Give the extent of all Plasmodium falciparum-infected red blood cells.
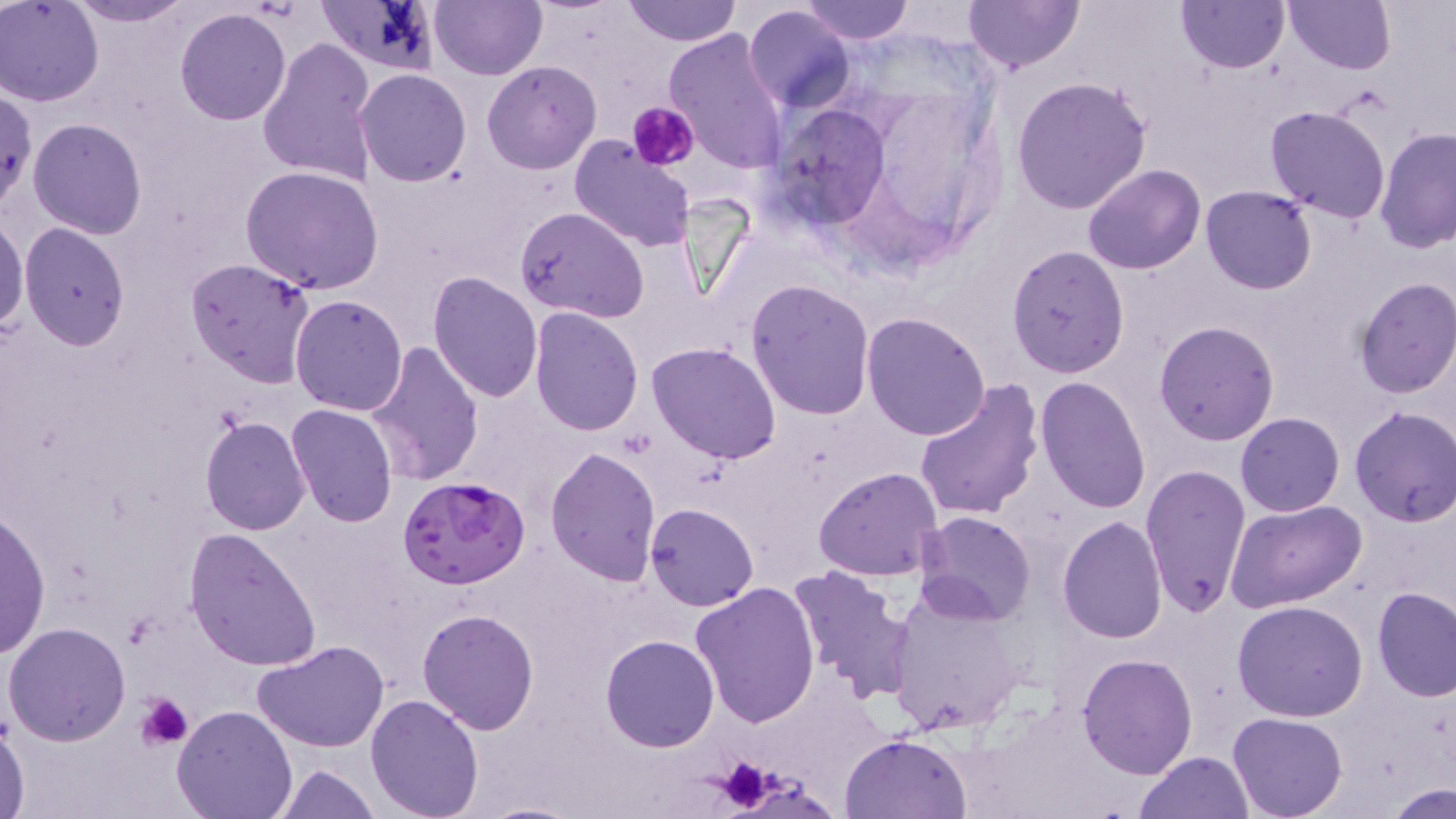

Approximate bounding boxes as named x1/y1/x2/y2 corners in pixels.
Plasmodium falciparum-infected red blood cells: (x1=397, y1=475, x2=530, y2=590).

slide-level diagnosis = Plasmodium falciparum
uninfected red blood cell locations = approximate bounding boxes as named x1/y1/x2/y2 corners in pixels: (x1=1, y1=0, x2=104, y2=105), (x1=68, y1=0, x2=193, y2=26), (x1=429, y1=0, x2=545, y2=81), (x1=623, y1=0, x2=741, y2=46), (x1=802, y1=0, x2=913, y2=44), (x1=964, y1=0, x2=1085, y2=74), (x1=1176, y1=0, x2=1289, y2=73), (x1=1285, y1=0, x2=1395, y2=74), (x1=742, y1=4, x2=857, y2=114), (x1=173, y1=8, x2=293, y2=126), (x1=662, y1=26, x2=790, y2=174), (x1=257, y1=36, x2=379, y2=188), (x1=482, y1=60, x2=601, y2=174), (x1=355, y1=69, x2=471, y2=186), (x1=1012, y1=76, x2=1153, y2=214), (x1=0, y1=88, x2=36, y2=212), (x1=769, y1=103, x2=895, y2=231), (x1=1265, y1=105, x2=1392, y2=223), (x1=28, y1=118, x2=146, y2=239), (x1=1376, y1=127, x2=1456, y2=254), (x1=568, y1=137, x2=694, y2=252), (x1=241, y1=164, x2=385, y2=294), (x1=1083, y1=164, x2=1206, y2=275), (x1=1200, y1=185, x2=1319, y2=295), (x1=515, y1=205, x2=648, y2=323), (x1=0, y1=215, x2=28, y2=337), (x1=18, y1=223, x2=130, y2=349), (x1=1006, y1=244, x2=1128, y2=378), (x1=186, y1=258, x2=315, y2=388), (x1=427, y1=270, x2=544, y2=403), (x1=1353, y1=277, x2=1456, y2=399), (x1=747, y1=278, x2=876, y2=419), (x1=289, y1=295, x2=408, y2=417), (x1=530, y1=305, x2=644, y2=434), (x1=861, y1=311, x2=992, y2=442), (x1=1154, y1=320, x2=1280, y2=445), (x1=365, y1=342, x2=485, y2=484), (x1=648, y1=343, x2=781, y2=464), (x1=1034, y1=376, x2=1153, y2=514), (x1=912, y1=380, x2=1044, y2=523), (x1=285, y1=404, x2=400, y2=528), (x1=1349, y1=405, x2=1456, y2=527), (x1=1236, y1=412, x2=1345, y2=517), (x1=201, y1=416, x2=312, y2=536), (x1=544, y1=447, x2=662, y2=587), (x1=1139, y1=463, x2=1253, y2=618), (x1=813, y1=466, x2=946, y2=581), (x1=1225, y1=500, x2=1369, y2=612), (x1=645, y1=502, x2=760, y2=610), (x1=1, y1=509, x2=50, y2=659), (x1=915, y1=510, x2=1037, y2=624), (x1=1057, y1=516, x2=1168, y2=643), (x1=183, y1=526, x2=322, y2=671), (x1=786, y1=564, x2=916, y2=704), (x1=690, y1=582, x2=822, y2=728), (x1=881, y1=586, x2=1030, y2=739), (x1=1373, y1=586, x2=1456, y2=701), (x1=1232, y1=599, x2=1367, y2=721), (x1=416, y1=607, x2=541, y2=733), (x1=3, y1=622, x2=131, y2=745), (x1=600, y1=634, x2=719, y2=752), (x1=253, y1=640, x2=389, y2=750), (x1=1078, y1=652, x2=1197, y2=777), (x1=366, y1=694, x2=485, y2=819), (x1=171, y1=705, x2=297, y2=819), (x1=1229, y1=713, x2=1346, y2=819), (x1=0, y1=714, x2=30, y2=818), (x1=839, y1=733, x2=970, y2=818), (x1=1136, y1=750, x2=1254, y2=818), (x1=274, y1=764, x2=380, y2=819), (x1=1383, y1=784, x2=1454, y2=819), (x1=476, y1=800, x2=589, y2=819)
platelet locations = approximate bounding boxes as named x1/y1/x2/y2 corners in pixels: (x1=629, y1=101, x2=699, y2=171), (x1=137, y1=692, x2=193, y2=749), (x1=698, y1=757, x2=800, y2=815)
stain = May-Grünwald-Giemsa
modality = optical microscopy
image size = 1456×819 pixels
preparation = thin blood smear
magnification = 1000x
field of view = single